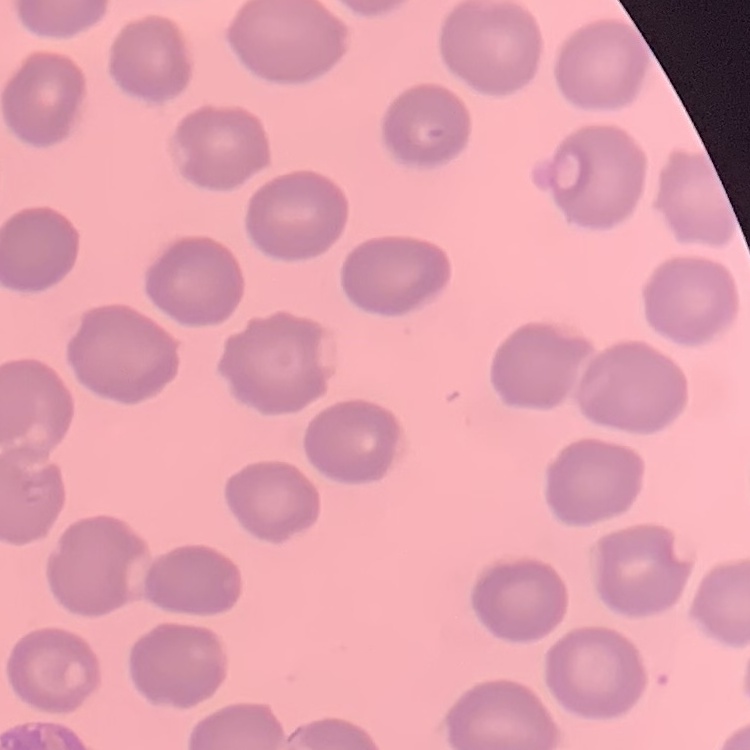 The erythrocytes show no rouleaux formation. Thin blood smear. Stained with either Field's or Giemsa. Square crop of a larger photomicrograph.